Outline each Plasmodium parasite.
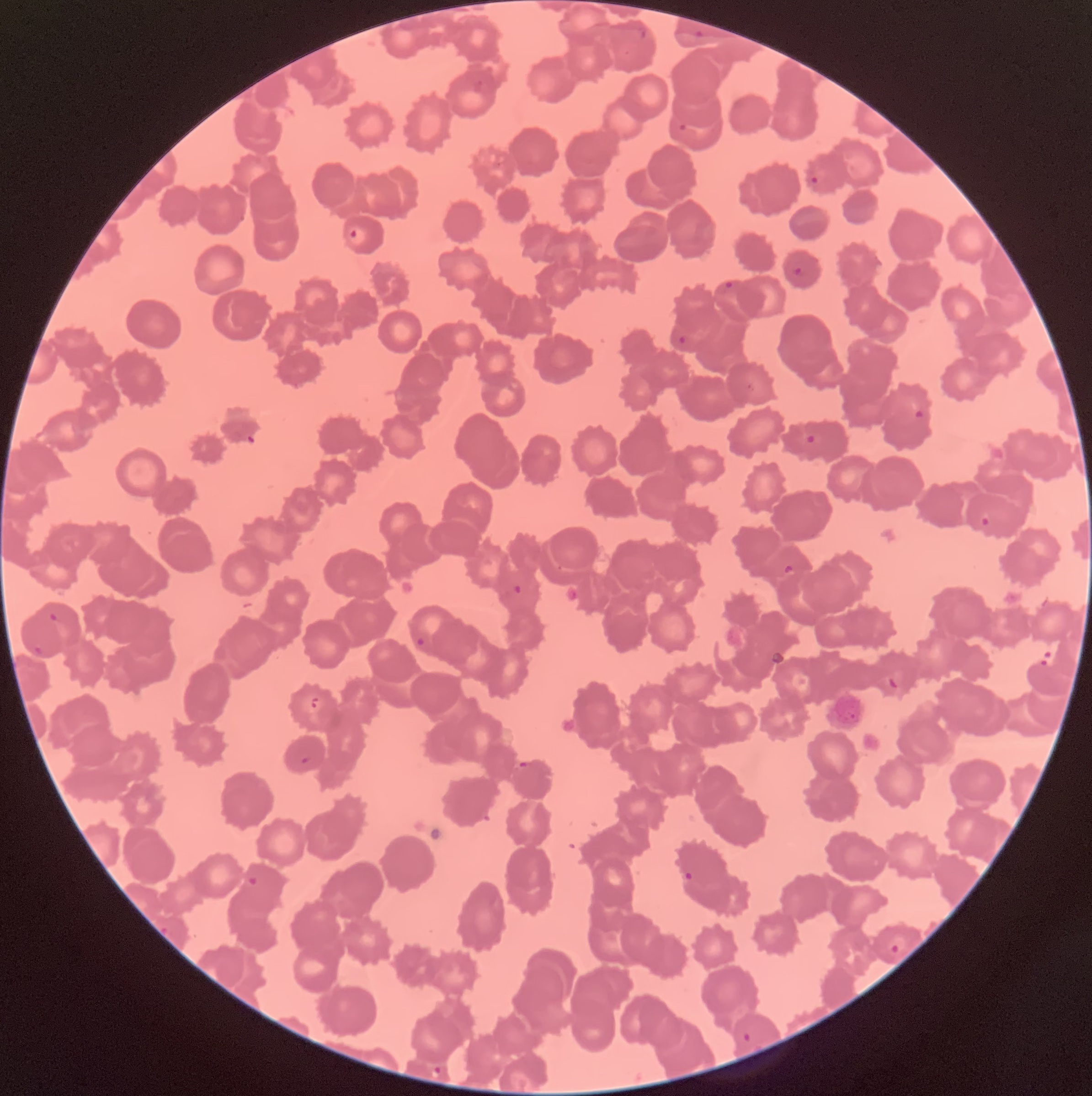

Approximate bounding boxes as (x1, y1, x2, y2) in pixels.
Plasmodium parasites: (637, 27, 646, 38), (695, 29, 703, 38), (472, 79, 483, 95), (679, 123, 689, 132), (493, 162, 501, 168), (810, 176, 819, 185), (350, 228, 358, 240), (792, 267, 803, 276), (724, 280, 734, 290), (677, 335, 687, 345), (747, 382, 756, 392), (913, 409, 925, 419), (804, 433, 817, 445), (980, 515, 991, 527), (784, 563, 794, 574), (513, 584, 524, 595), (49, 613, 58, 621), (415, 637, 426, 647), (33, 644, 43, 655), (887, 674, 900, 690), (311, 697, 318, 710), (300, 756, 311, 765), (518, 761, 527, 767), (683, 870, 694, 883), (245, 873, 259, 885), (160, 925, 169, 936), (888, 933, 908, 955), (743, 1033, 752, 1041), (432, 1066, 442, 1078).

red blood cell morphology = rouleaux formation
modality = light microscopy
image size = 1092×1096 pixels
preparation = thin blood smear